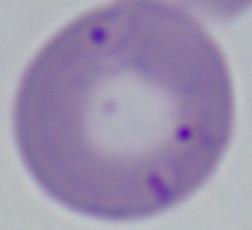
modality: micrograph
identification: Babesia
magnification: 1000x